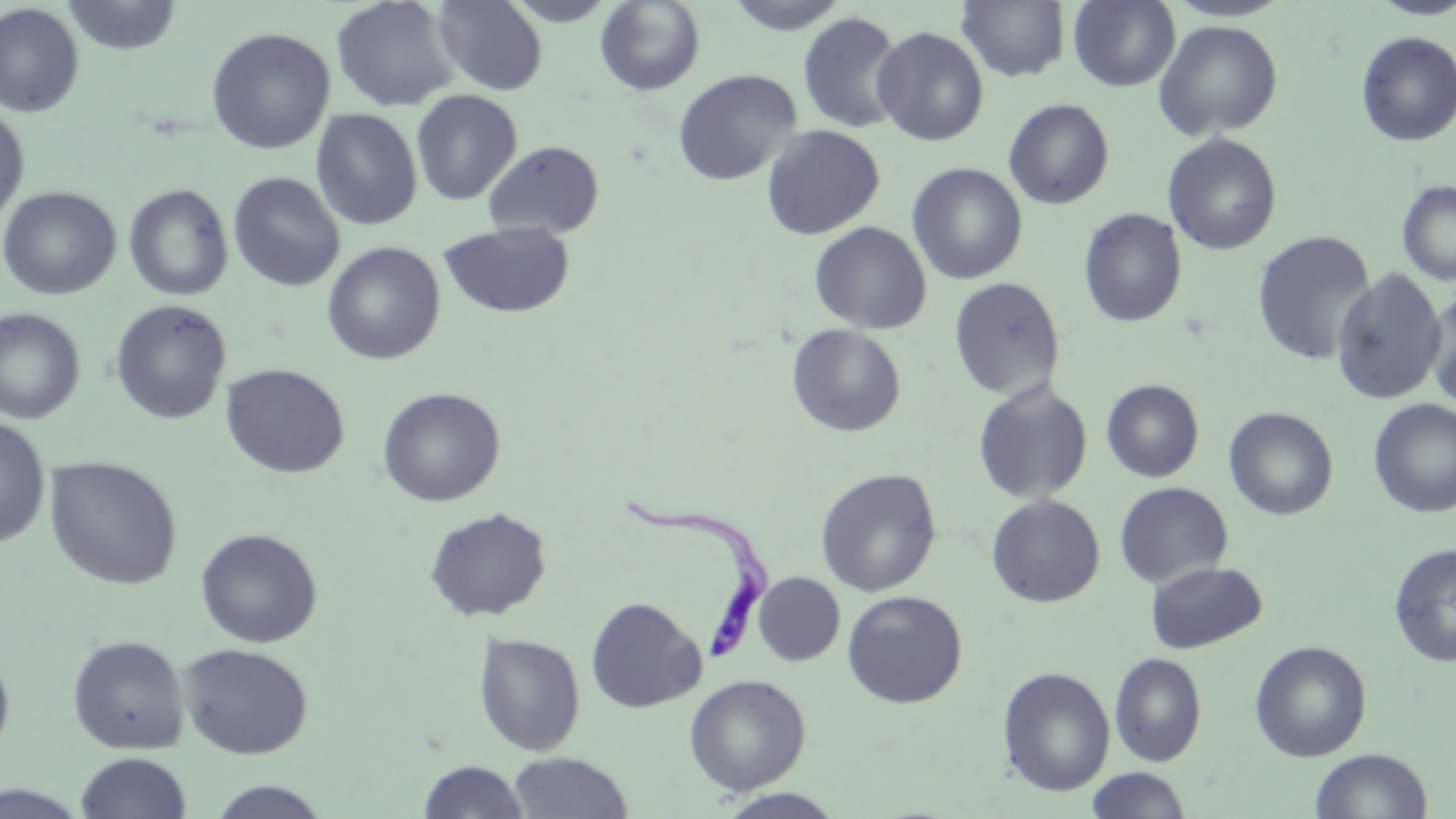

Summary:
  - Coordinate format: approximate bounding boxes as (x1, y1, x2, y2) in pixels
  - Trypanosoma brucei locations: (619, 495, 770, 663)
  - Uninfected red blood cell locations: (61, 0, 183, 56), (432, 0, 548, 96), (502, 0, 620, 26), (724, 0, 851, 35), (956, 0, 1071, 82), (1068, 0, 1181, 92), (1164, 0, 1292, 23), (1368, 0, 1456, 20), (330, 1, 460, 112), (594, 1, 706, 96), (0, 3, 84, 118), (797, 12, 905, 134), (1153, 20, 1284, 141), (871, 26, 989, 146), (205, 27, 335, 155), (1355, 31, 1456, 147), (672, 69, 801, 187), (411, 90, 522, 206), (1004, 99, 1114, 209), (0, 105, 30, 225), (311, 108, 423, 231), (761, 125, 885, 240), (1163, 134, 1282, 256), (483, 140, 605, 239), (907, 162, 1028, 285), (228, 171, 345, 292), (1397, 179, 1456, 287), (123, 183, 234, 302), (0, 186, 121, 300), (1078, 208, 1187, 328), (438, 221, 575, 320), (809, 221, 932, 334), (1252, 231, 1375, 366), (321, 242, 445, 365), (1331, 268, 1448, 405), (948, 277, 1066, 401), (1425, 288, 1456, 412), (110, 299, 232, 425), (0, 308, 85, 425), (786, 324, 906, 437), (220, 363, 350, 479), (1101, 379, 1204, 482), (972, 380, 1093, 504), (377, 387, 504, 507), (1368, 398, 1456, 518), (1224, 407, 1338, 521), (0, 415, 51, 548), (44, 456, 182, 590), (815, 468, 941, 597), (833, 470, 956, 708), (1114, 482, 1233, 589), (986, 494, 1105, 608), (424, 507, 551, 622), (195, 528, 322, 648), (1388, 542, 1456, 667), (1144, 560, 1268, 654), (753, 572, 845, 666), (841, 590, 968, 709), (585, 596, 705, 714), (473, 632, 586, 756), (67, 634, 189, 755), (1251, 641, 1373, 761), (177, 642, 313, 759), (0, 649, 15, 763), (1109, 653, 1207, 766), (997, 667, 1115, 797), (684, 673, 811, 796), (1310, 748, 1433, 818), (74, 752, 192, 819), (507, 752, 633, 818), (417, 760, 530, 818), (1085, 767, 1192, 818), (205, 780, 333, 819), (0, 784, 91, 819), (714, 788, 848, 819)
  - Slide-level diagnosis: Trypanosoma brucei
  - Field of view: single
  - Magnification: 1000x
  - Stain: May-Grünwald-Giemsa
  - Modality: optical microscopy
  - Image size: 1456×819 pixels
  - Preparation: thin blood film